Outline each blood parasite and name the species.
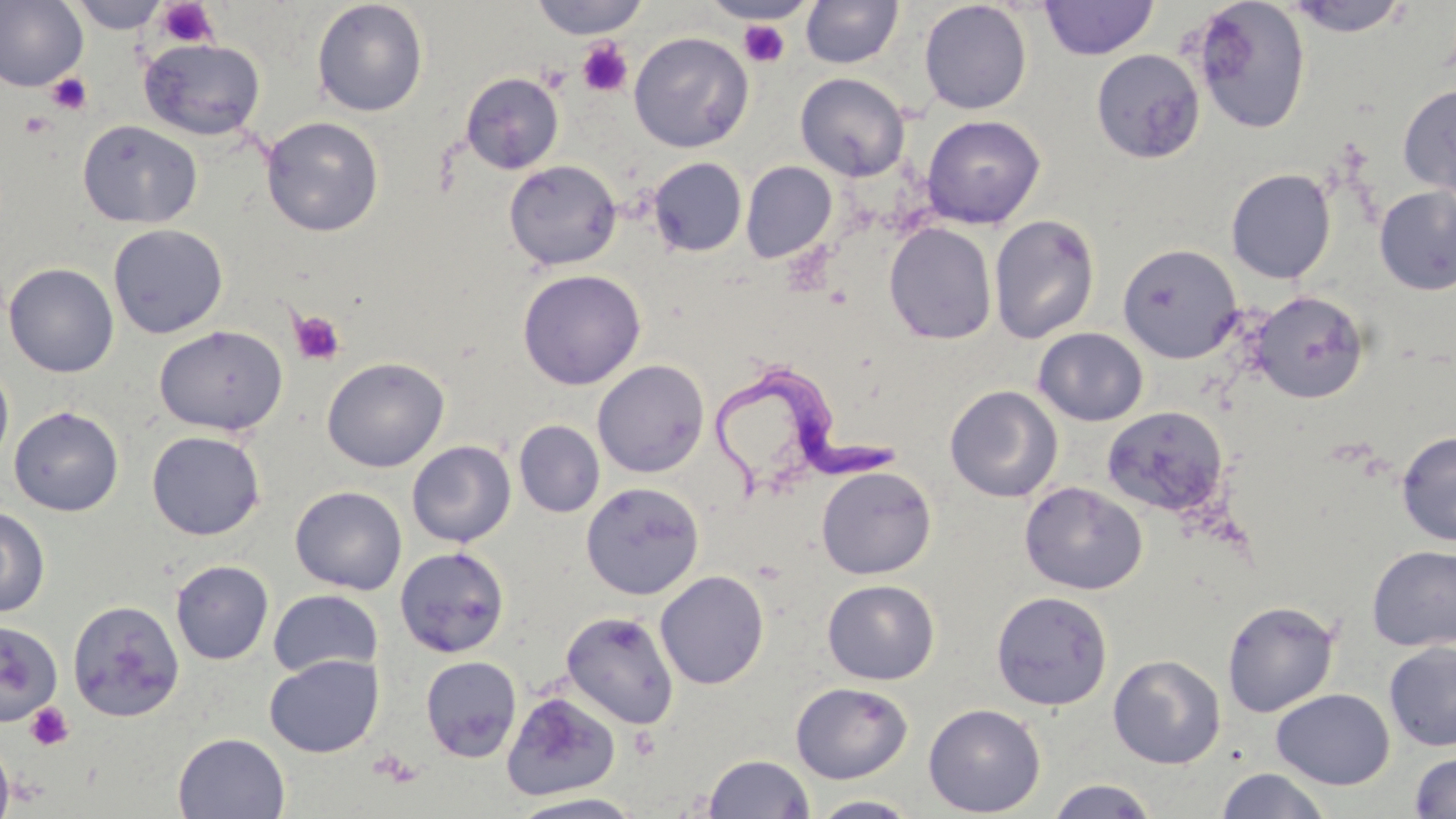
Approximate bounding boxes as (x1, y1, x2, y2) in pixels.
Trypanosoma brucei: (712, 362, 900, 499).
No Plasmodium falciparum, Plasmodium ovale, Plasmodium malariae, Plasmodium vivax, or Babesia divergens observed.

Summary:
  - Uninfected red blood cell locations: (0, 0, 88, 92), (68, 0, 168, 33), (311, 0, 428, 117), (527, 0, 651, 39), (1191, 0, 1312, 134), (1283, 0, 1415, 37), (702, 1, 817, 24), (799, 1, 904, 68), (918, 1, 1033, 114), (1039, 1, 1158, 59), (628, 31, 754, 153), (138, 36, 266, 142), (1090, 49, 1205, 163), (460, 72, 564, 175), (795, 72, 909, 181), (1397, 83, 1456, 198), (921, 114, 1046, 228), (261, 116, 384, 237), (77, 120, 203, 229), (647, 157, 747, 257), (503, 159, 622, 270), (741, 161, 837, 263), (1225, 168, 1336, 284), (1373, 186, 1456, 295), (988, 214, 1101, 345), (108, 223, 228, 339), (883, 223, 997, 344), (1117, 243, 1243, 363), (4, 262, 119, 377), (516, 268, 647, 390), (1250, 290, 1370, 403), (153, 324, 288, 436), (1033, 327, 1148, 426), (321, 357, 449, 472), (592, 359, 710, 478), (0, 361, 14, 470), (944, 385, 1063, 502), (9, 406, 124, 516), (1102, 406, 1229, 518), (514, 420, 604, 518), (146, 430, 265, 540), (1396, 430, 1456, 546), (407, 440, 516, 548), (816, 465, 937, 579), (580, 481, 704, 600), (1020, 481, 1147, 595), (290, 485, 408, 595), (0, 506, 50, 618), (1366, 544, 1456, 651), (394, 546, 510, 658), (170, 560, 274, 665), (655, 570, 770, 689), (822, 579, 940, 685), (268, 589, 383, 678), (990, 590, 1113, 710), (66, 599, 186, 722), (1221, 599, 1340, 717), (560, 610, 680, 729), (0, 620, 62, 725), (1383, 642, 1456, 751), (264, 653, 383, 758), (1108, 654, 1226, 768), (420, 655, 522, 762), (791, 681, 912, 783), (1271, 688, 1395, 789), (502, 691, 620, 801), (923, 703, 1046, 817), (172, 732, 290, 818), (0, 735, 15, 819), (1408, 751, 1456, 818), (703, 753, 815, 818), (1216, 768, 1331, 819), (1046, 778, 1158, 818), (507, 792, 647, 818), (808, 794, 923, 818)
  - Platelet locations: (156, 1, 219, 49), (738, 20, 790, 67), (577, 39, 634, 96), (47, 73, 92, 115), (19, 111, 53, 139), (290, 310, 346, 366), (26, 703, 74, 751)
  - Slide-level diagnosis: Trypanosoma brucei
  - Stain: May-Grünwald-Giemsa
  - Magnification: 1000x
  - Image size: 1456×819 pixels
  - Field of view: one of a larger specimen
  - Preparation: thin blood film
  - Modality: optical microscopy